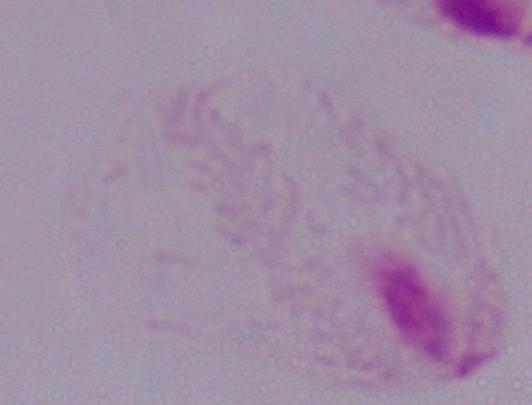
Summary:
  - Magnification: 1000x
  - Modality: micrograph
  - Identification: trichomonad